Assess this cell for malaria.
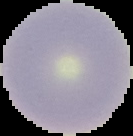
It is uninfected.

Image is 133×136 pixels. The area outside the segmented cell region is set to black. From a thin blood smear.